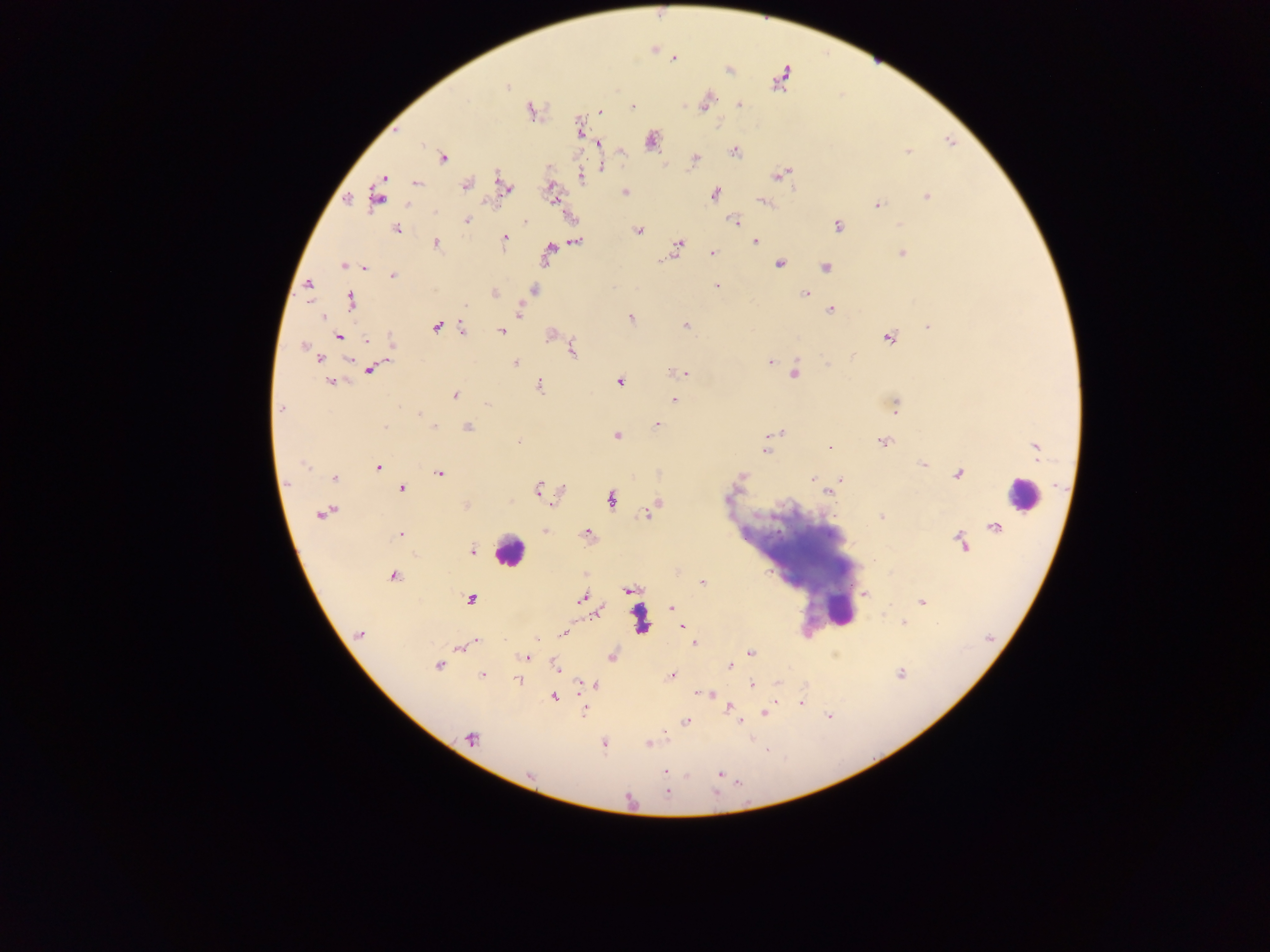

leukocyte_locations: 'approximate centers as {x, y} in pixels: {1021, 493}, {509, 551}, {837, 609}, {640, 619}'
country: Ghana
capture: mobile-phone photograph through a microscope
field_of_view: single
malaria_parasite_locations: 'approximate centers as {x, y} in pixels: {674, 58}, {781, 78}, {507, 87}, {705, 102}, {739, 105}, {633, 106}, {530, 110}, {600, 112}, {580, 129}, {651, 140}, {598, 143}, {734, 151}, {907, 151}, {443, 159}, {696, 159}, {601, 167}, {779, 175}, {581, 178}, {417, 182}, {465, 184}, {503, 185}, {625, 192}, {715, 194}, {377, 195}, {552, 196}, {926, 196}, {763, 202}, {877, 205}, {435, 212}, {467, 221}, {525, 221}, {734, 221}, {901, 225}, {837, 226}, {397, 229}, {637, 231}, {505, 239}, {755, 241}, {577, 242}, {436, 243}, {679, 243}, {548, 253}, {713, 253}, {902, 253}, {662, 259}, {780, 263}, {343, 266}, {364, 267}, {825, 267}, {393, 275}, {309, 285}, {716, 286}, {535, 291}, {494, 293}, {805, 293}, {351, 300}, {830, 309}, {520, 311}, {322, 317}, {631, 319}, {685, 325}, {436, 326}, {928, 327}, {462, 328}, {502, 331}, {339, 336}, {889, 337}, {367, 340}, {391, 344}, {304, 347}, {573, 350}, {852, 356}, {320, 358}, {349, 360}, {770, 362}, {515, 363}, {828, 365}, {370, 370}, {682, 373}, {795, 374}, {619, 381}, {330, 382}, {540, 386}, {455, 395}, {674, 400}, {487, 404}, {895, 405}, {280, 409}, {419, 414}, {657, 425}, {385, 427}, {434, 427}, {467, 427}, {781, 432}, {617, 436}, {518, 442}, {884, 442}, {829, 447}, {1034, 448}, {764, 451}, {304, 464}, {923, 464}, {378, 467}, {440, 473}, {958, 474}, {742, 477}, {335, 478}, {812, 478}, {840, 479}, {402, 489}, {538, 489}, {828, 493}, {726, 497}, {611, 500}, {466, 506}, {647, 513}, {321, 514}, {882, 517}, {545, 531}, {586, 533}, {399, 534}, {961, 541}, {472, 551}, {393, 576}, {702, 583}, {629, 590}, {864, 594}, {470, 599}, {582, 599}, {921, 602}, {672, 607}, {903, 623}, {683, 626}, {360, 634}, {562, 634}, {536, 638}, {476, 642}, {694, 643}, {459, 647}, {750, 652}, {526, 657}, {611, 657}, {439, 665}, {729, 666}, {556, 668}, {900, 674}, {482, 675}, {672, 675}, {517, 679}, {581, 682}, {778, 683}, {752, 684}, {594, 685}, {710, 695}, {554, 698}, {801, 704}, {729, 707}, {584, 709}, {766, 713}, {686, 721}, {739, 721}, {472, 739}, {604, 744}, {648, 744}, {664, 771}, {720, 774}, {666, 792}'
image_size: 1270×952 pixels
preparation: thick blood film